Assess this cell for malaria.
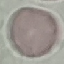
Uninfected.

Summary:
  - Capture: smartphone through the microscope eyepiece
  - Image type: automatically extracted cell patch, resized to 64 × 64 pixels
  - Preparation: thin blood smear
  - Stain: Giemsa